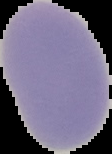

Image is 112×154 pixels. From a thin blood film. Malaria status: uninfected. The area outside the segmented cell region is set to black.